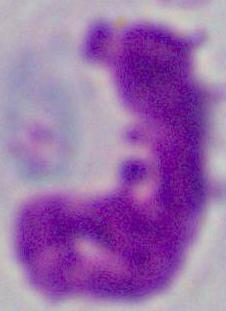

Captured at 1000x magnification. Micrograph. A leukocyte is seen.